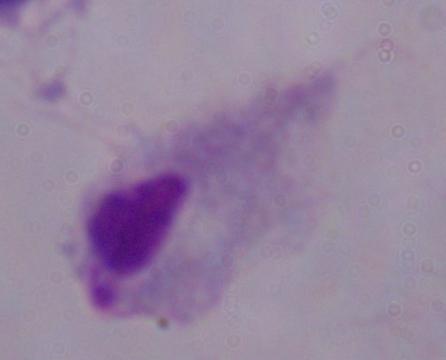

Summary:
  - Identification: trichomonad
  - Magnification: 1000x
  - Modality: photomicrograph